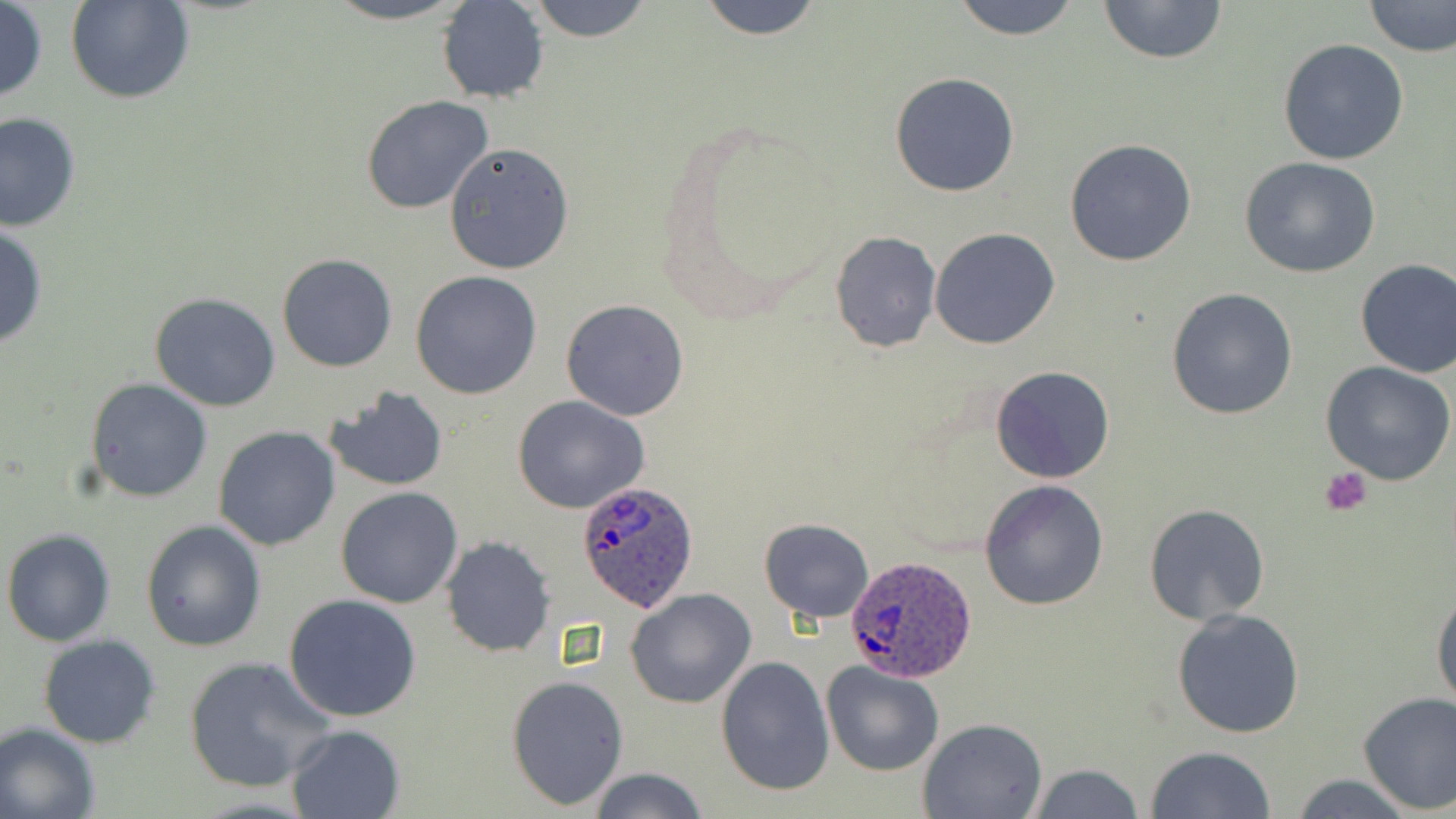
Approximate bounding boxes as [x1, y1, x2, y2] in pixels. Uninfected red blood cell locations: [66, 0, 194, 104], [316, 0, 474, 25], [526, 0, 654, 42], [695, 0, 825, 39], [949, 0, 1084, 39], [1097, 0, 1226, 64], [1362, 0, 1455, 58], [0, 1, 47, 103], [437, 1, 550, 102], [1277, 39, 1409, 165], [890, 73, 1020, 196], [361, 96, 494, 216], [0, 111, 81, 232], [1065, 138, 1197, 267], [444, 142, 574, 275], [1239, 157, 1383, 279], [0, 222, 48, 350], [930, 228, 1060, 348], [831, 232, 940, 352], [277, 254, 398, 372], [1354, 258, 1455, 379], [410, 270, 543, 398], [1167, 288, 1298, 419], [149, 292, 281, 411], [560, 299, 690, 421], [1322, 362, 1456, 486], [989, 365, 1115, 484], [86, 378, 213, 502], [321, 385, 448, 492], [513, 395, 651, 514], [213, 425, 342, 551], [979, 480, 1110, 611], [335, 487, 463, 609], [1143, 502, 1272, 624], [758, 518, 875, 622], [142, 519, 268, 652], [2, 528, 117, 647], [441, 536, 555, 658], [1431, 582, 1456, 711], [625, 588, 757, 709], [284, 593, 422, 721], [1172, 608, 1306, 739], [37, 635, 162, 750], [184, 654, 335, 793], [715, 654, 836, 797], [822, 662, 944, 777], [507, 675, 630, 811], [1358, 691, 1456, 815], [918, 717, 1047, 819], [0, 723, 101, 819], [286, 724, 405, 819], [1144, 744, 1277, 819], [1026, 763, 1145, 818], [588, 767, 708, 819], [1288, 774, 1422, 818]. Platelet locations: [1318, 465, 1373, 516]. Plasmodium ovale-infected red blood cell locations: [577, 480, 699, 611], [844, 554, 979, 682]. Slide-level diagnosis: Plasmodium ovale. May-Grünwald-Giemsa stain. Image is 1456×819 pixels. 1000x magnification. Optical microscopy. Thin blood smear. Single field of view.